Assess the morphology of the erythrocytes.
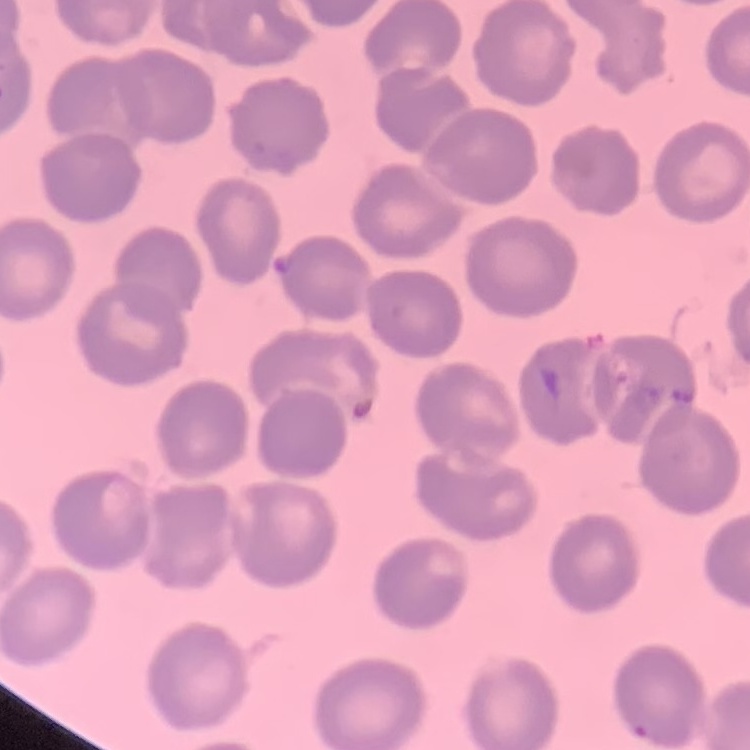
No rouleaux formation.

Thin blood smear. One tile cut from a larger photomicrograph. Field's or Giemsa stain.